Locate every blood parasite and identify its species.
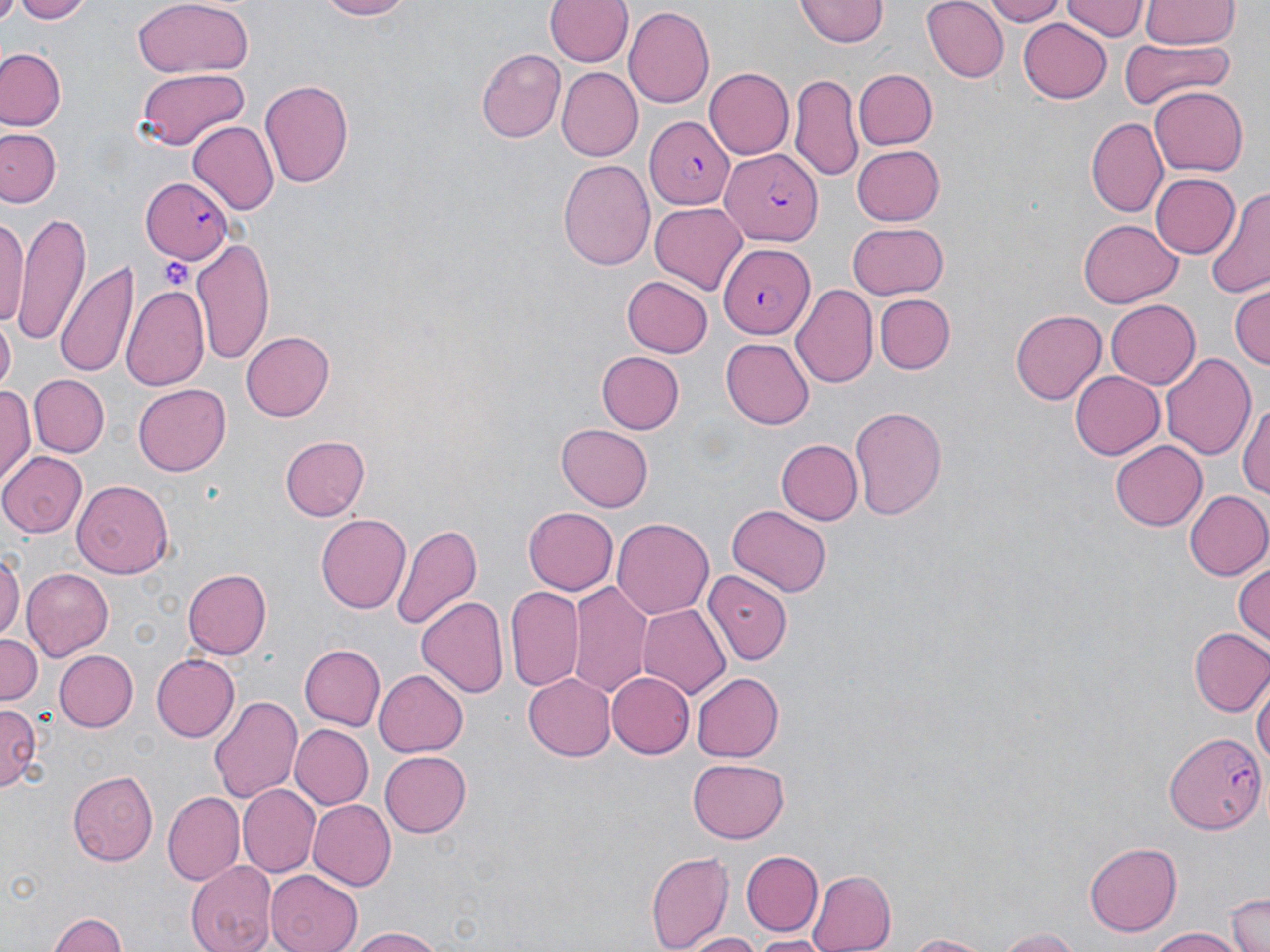
Approximate bounding boxes as (x1, y1, x2, y2) in pixels.
Plasmodium falciparum-infected red blood cells: (645, 117, 735, 209), (716, 143, 823, 249), (140, 178, 234, 263), (719, 240, 814, 336), (1161, 729, 1268, 835).
No Plasmodium ovale, Plasmodium malariae, Plasmodium vivax, Babesia divergens, or Trypanosoma brucei observed.

Uninfected red blood cell locations: (9, 0, 97, 23), (310, 0, 413, 20), (797, 0, 889, 48), (920, 0, 1007, 82), (983, 0, 1069, 26), (1061, 0, 1144, 42), (130, 1, 255, 79), (545, 1, 633, 68), (1141, 1, 1240, 49), (625, 7, 714, 109), (1018, 19, 1113, 103), (1119, 40, 1235, 111), (0, 48, 64, 131), (476, 49, 565, 142), (134, 68, 249, 149), (705, 68, 795, 158), (853, 68, 936, 148), (557, 69, 643, 159), (791, 75, 862, 181), (260, 77, 354, 189), (1150, 87, 1248, 175), (1089, 116, 1170, 217), (187, 121, 278, 216), (0, 127, 60, 209), (850, 144, 943, 225), (559, 159, 656, 272), (1151, 173, 1240, 260), (1204, 190, 1270, 301), (650, 202, 749, 295), (12, 210, 90, 341), (0, 211, 27, 331), (1079, 218, 1180, 308), (847, 223, 947, 298), (192, 237, 275, 361), (57, 261, 139, 379), (621, 275, 712, 357), (790, 282, 876, 389), (120, 283, 210, 393), (1230, 285, 1269, 372), (874, 292, 954, 373), (1104, 299, 1199, 388), (1012, 310, 1106, 402), (0, 322, 15, 391), (240, 330, 334, 421), (722, 338, 814, 428), (596, 351, 685, 434), (1160, 351, 1258, 461), (1070, 371, 1164, 459), (29, 374, 110, 458), (134, 381, 230, 473), (0, 385, 35, 486), (1239, 397, 1270, 507), (848, 402, 945, 518), (556, 423, 652, 512), (279, 435, 368, 521), (775, 438, 862, 524), (1111, 440, 1209, 530), (0, 450, 85, 535), (71, 479, 173, 580), (1183, 490, 1270, 581), (725, 505, 830, 597), (521, 506, 617, 596), (317, 513, 409, 614), (611, 517, 714, 621), (392, 521, 482, 630), (0, 549, 21, 648), (1232, 557, 1270, 650), (698, 565, 787, 688), (22, 567, 114, 661), (183, 567, 272, 658), (570, 580, 654, 698), (506, 586, 582, 691), (418, 596, 508, 700), (639, 605, 730, 699), (1189, 627, 1270, 717), (0, 631, 42, 704), (299, 643, 385, 730), (53, 649, 137, 731), (151, 653, 240, 742), (374, 670, 468, 757), (1252, 670, 1268, 781), (523, 673, 615, 760), (607, 673, 693, 757), (692, 673, 784, 761), (208, 694, 302, 805), (0, 702, 43, 795), (288, 724, 372, 810), (380, 750, 471, 838), (687, 758, 788, 843), (67, 771, 158, 865), (236, 784, 320, 878), (162, 791, 243, 885), (310, 800, 395, 890), (1085, 842, 1184, 934), (646, 847, 736, 952), (741, 850, 824, 936), (185, 859, 275, 952), (266, 869, 359, 952), (806, 869, 894, 952), (1225, 891, 1270, 952), (50, 910, 131, 952), (346, 926, 444, 952), (988, 927, 1088, 951), (1145, 927, 1245, 951), (683, 932, 765, 952), (894, 932, 1002, 951), (745, 934, 835, 951). Platelet locations: (160, 258, 192, 289). Slide-level diagnosis: Plasmodium falciparum. May-Grünwald-Giemsa-stained preparation. 1000x magnification. Light microscopy. Image is 1270×952 pixels. One field of a larger specimen. Thin blood smear.